Classify this cell by malaria status.
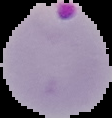

It is parasitized.

Summary:
  - Image size: 112×118 pixels
  - Image type: cell region segmented out of the field of view; surrounding area masked to black
  - Preparation: thin blood smear